Evaluate for malaria.
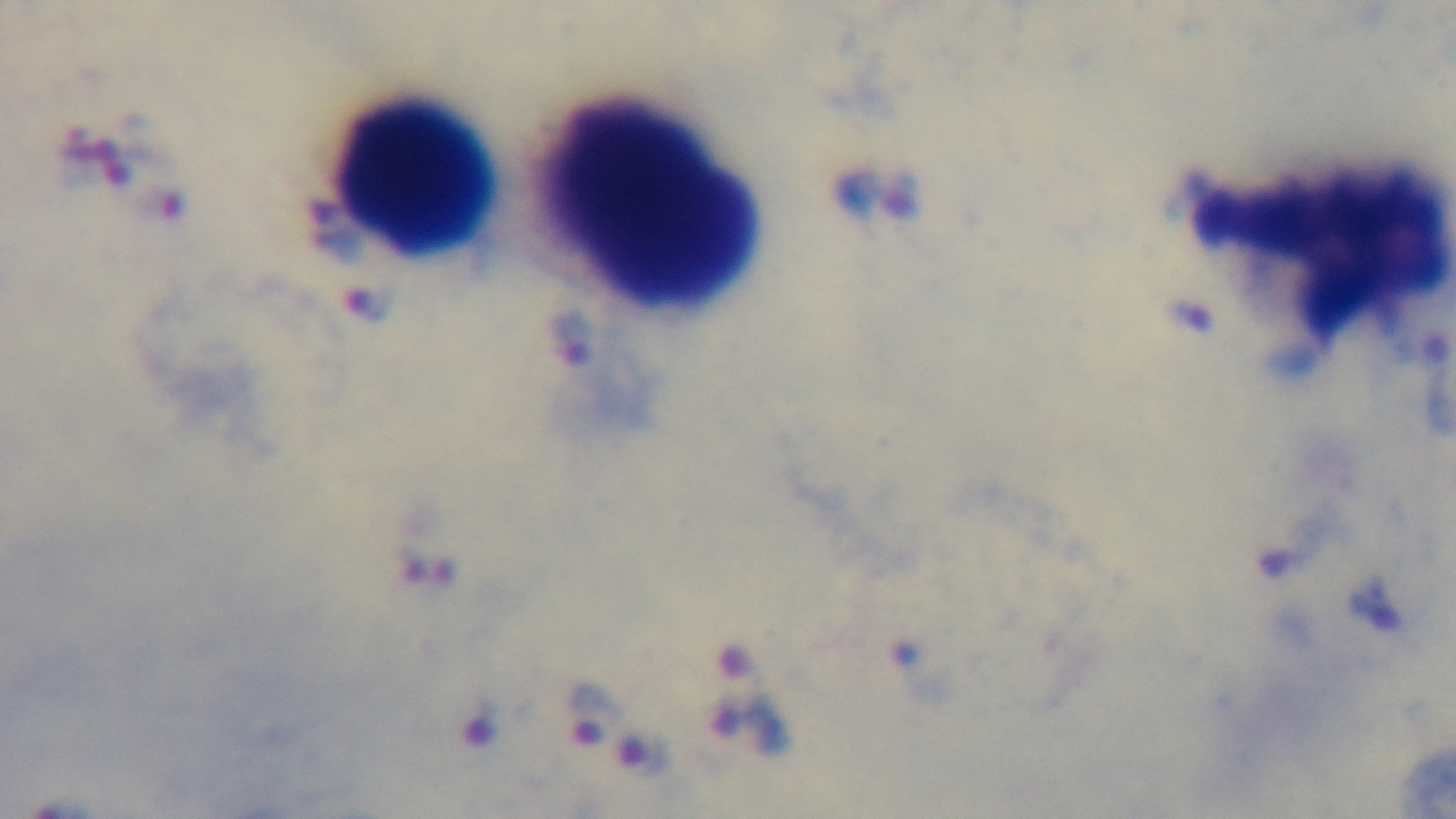

It is infected.

stain = Giemsa
field of view = one from the slide
objective = 100x oil immersion
capture = mounted 4K digital camera
preparation = thick blood film
modality = light microscopy